Mark where platelets are.
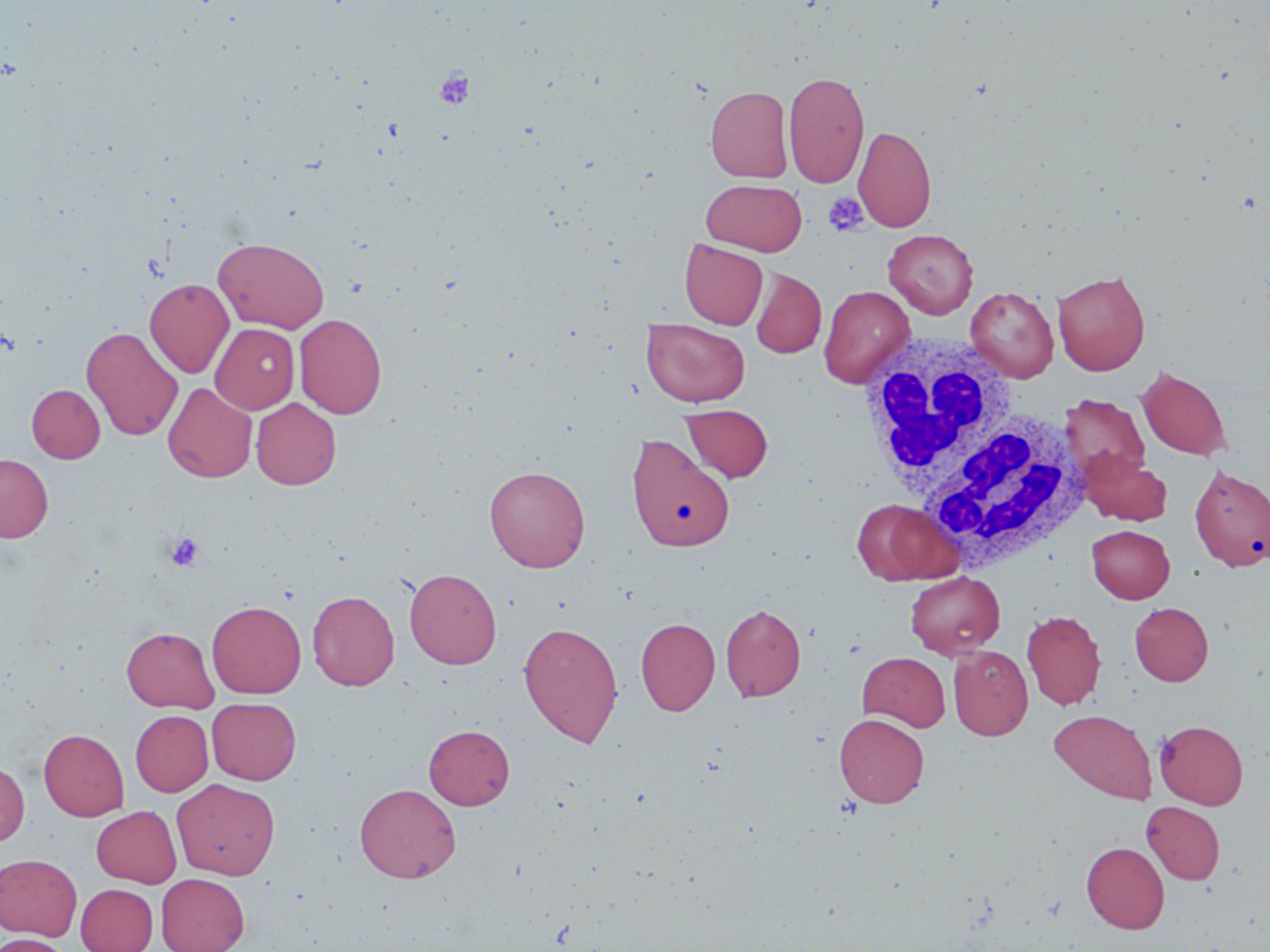

Approximate bounding boxes as (x1,y1)-(x2,y2) corner pairs in pixels.
Platelets: (434,69)-(475,108), (823,193)-(868,235), (165,532)-(203,571).

White blood cell locations: (857,335)-(1021,501), (904,408)-(1093,577). Uninfected red blood cell locations: (784,70)-(869,188), (706,86)-(793,182), (853,124)-(936,232), (701,179)-(807,256), (884,229)-(978,319), (214,236)-(329,333), (680,239)-(768,330), (751,268)-(826,358), (1052,269)-(1150,376), (145,278)-(234,378), (819,285)-(915,388), (966,287)-(1058,382), (294,314)-(386,418), (642,321)-(749,407), (211,323)-(300,413), (81,326)-(183,441), (1135,365)-(1232,461), (163,382)-(257,483), (27,384)-(104,463), (1060,394)-(1149,483), (251,398)-(341,489), (681,404)-(772,482), (626,434)-(734,551), (1079,450)-(1172,526), (0,453)-(53,542), (1189,463)-(1270,572), (484,465)-(590,572), (852,498)-(960,585), (1087,525)-(1174,603), (405,568)-(502,669), (905,571)-(1005,659), (308,590)-(399,690), (207,600)-(306,698), (1130,602)-(1213,685), (720,603)-(806,702), (1022,610)-(1106,710), (636,617)-(720,715), (518,621)-(623,748), (121,627)-(219,713), (948,645)-(1033,739), (858,652)-(950,731), (207,698)-(301,784), (1049,708)-(1157,803), (131,710)-(213,796), (834,714)-(929,808), (1154,720)-(1248,809), (424,724)-(515,810), (39,729)-(129,821), (0,762)-(29,846), (171,778)-(280,879), (354,783)-(461,883), (1141,801)-(1225,884), (92,806)-(181,887), (1081,841)-(1169,933), (0,854)-(82,940), (156,873)-(249,952), (76,883)-(158,952), (0,934)-(71,952). Slide-level diagnosis: negative for blood parasites. Captured at 1000x magnification. May-Grünwald-Giemsa-stained preparation. Thin blood smear. One field of a larger specimen. Image is 1270×952 pixels. Optical microscopy.